Classify this cell by malaria status.
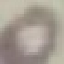
It is uninfected.

Summary:
  - Capture: smartphone through the microscope eyepiece
  - Image type: cell patch, automatically extracted from a larger field of view and resized to 64 × 64 pixels
  - Preparation: thin smear
  - Stain: Giemsa